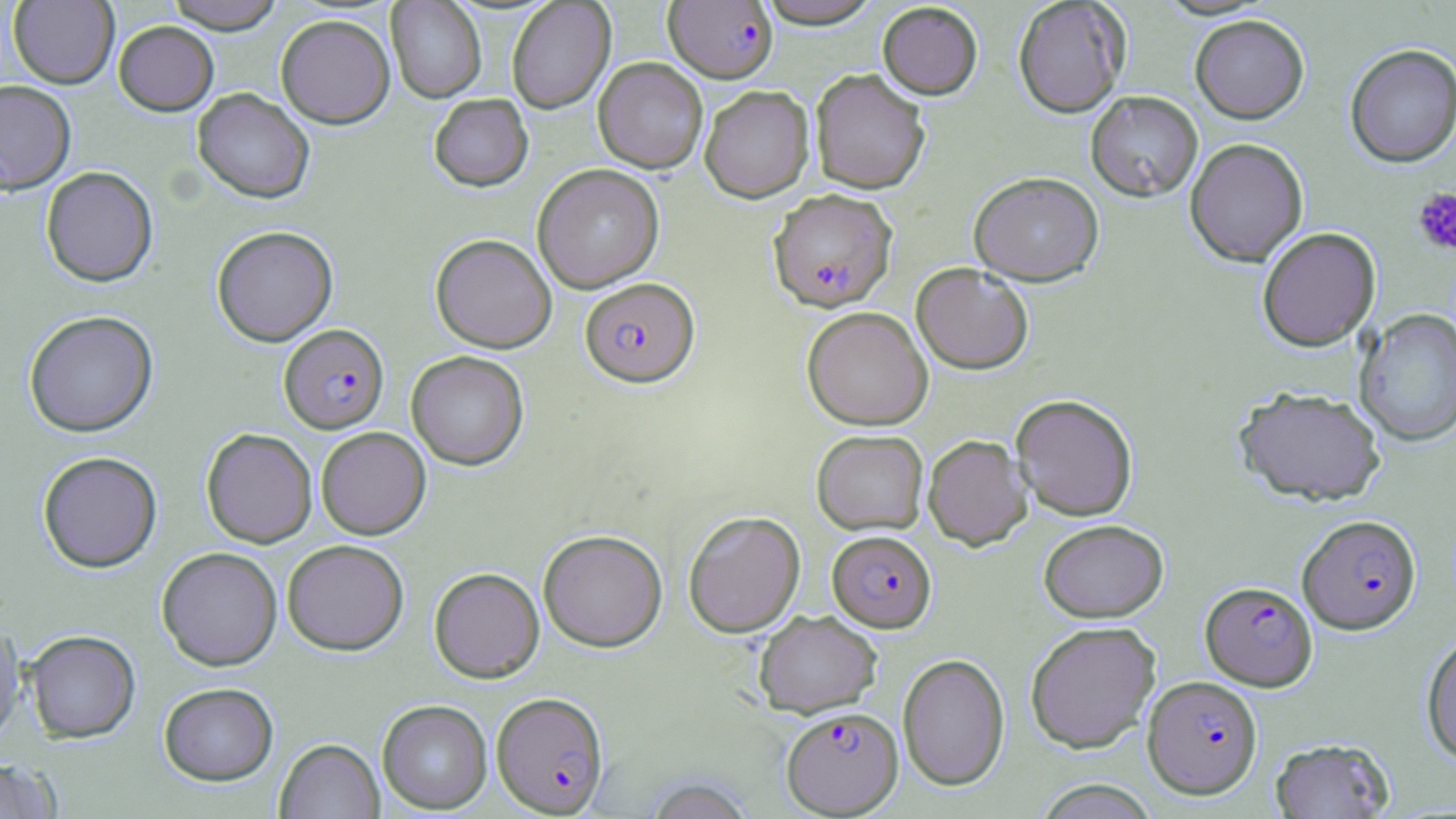
Approximate bounding boxes as (x1, y1, x2, y2) in pixels. Uninfected red blood cell locations: (164, 0, 285, 34), (753, 0, 886, 29), (1013, 0, 1131, 118), (8, 1, 119, 88), (386, 1, 487, 103), (506, 1, 616, 114), (877, 2, 983, 99), (276, 14, 395, 128), (1190, 14, 1309, 123), (113, 21, 219, 116), (1344, 43, 1456, 167), (593, 57, 708, 174), (810, 69, 930, 194), (1, 79, 76, 194), (700, 85, 814, 203), (192, 88, 315, 204), (1085, 90, 1202, 202), (428, 94, 533, 191), (1184, 137, 1309, 266), (533, 164, 664, 293), (41, 166, 158, 287), (969, 171, 1104, 285), (211, 225, 338, 346), (1257, 227, 1381, 352), (431, 234, 557, 353), (911, 263, 1034, 374), (802, 306, 933, 430), (1355, 308, 1456, 447), (24, 309, 158, 437), (406, 350, 529, 470), (1234, 386, 1386, 506), (1011, 393, 1138, 521), (316, 426, 430, 539), (201, 427, 317, 548), (811, 429, 929, 534), (923, 434, 1032, 550), (38, 451, 162, 572), (683, 510, 805, 637), (1038, 519, 1168, 622), (538, 529, 667, 651), (282, 539, 409, 655), (156, 547, 282, 670), (429, 567, 544, 683), (754, 609, 882, 717), (1024, 621, 1161, 752), (0, 624, 25, 745), (23, 629, 141, 743), (1420, 633, 1456, 764), (897, 653, 1010, 791), (159, 682, 278, 785), (377, 700, 492, 813), (1269, 737, 1395, 818), (274, 738, 385, 818), (0, 758, 62, 819), (1034, 780, 1163, 818). Plasmodium falciparum-infected red blood cell locations: (664, 1, 778, 83), (769, 188, 897, 312), (580, 277, 700, 386), (280, 324, 388, 433), (1297, 514, 1421, 634), (827, 530, 936, 631), (1200, 580, 1318, 691), (1143, 675, 1263, 798), (492, 691, 609, 816), (782, 706, 903, 816). Platelet locations: (1412, 187, 1456, 257). Slide-level diagnosis: Plasmodium falciparum. Light microscopy. Single field of view. Thin blood smear. Image is 1456×819 pixels. May-Grünwald-Giemsa stain. Captured at 1000x magnification.